State which parasite is depicted.
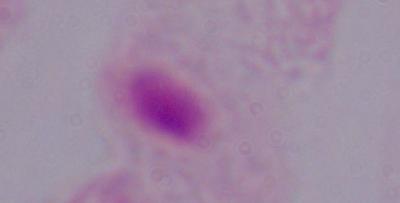
This is a trichomonad.

magnification = 1000x
modality = photomicrograph